Name the parasite shown.
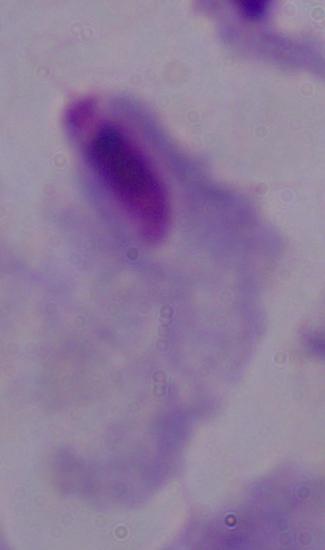

This is a trichomonad.

Captured at 1000x magnification. Micrograph.